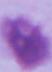
identification = red blood cell
modality = micrograph
magnification = 1000x